State the blood parasite species.
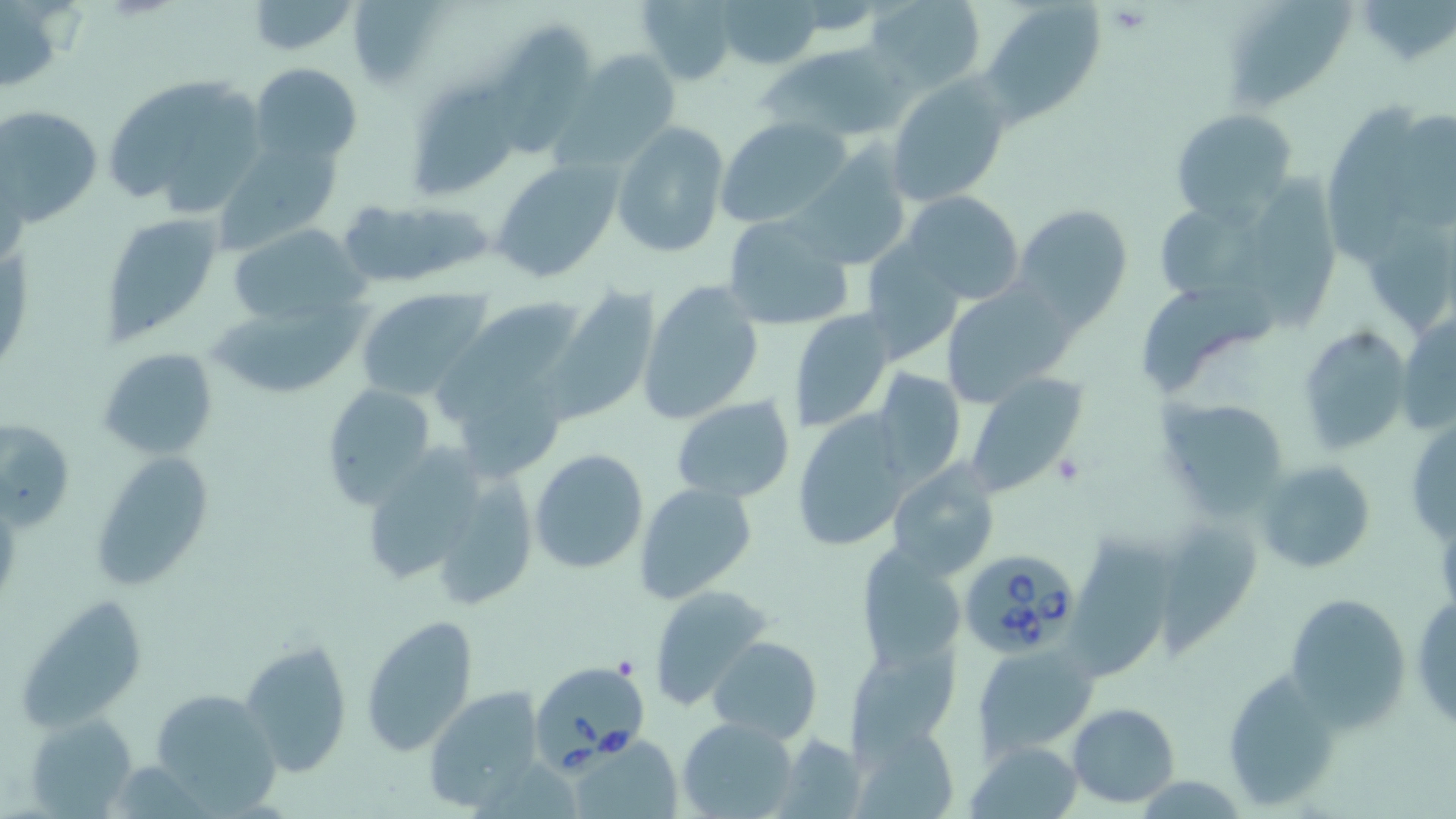
Babesia divergens.

Summary:
  - Coordinate format: approximate bounding boxes as (x1, y1, x2, y2) in pixels
  - Uninfected red blood cell locations: (348, 0, 449, 88), (635, 0, 742, 85), (716, 0, 825, 71), (865, 0, 988, 91), (1220, 0, 1358, 114), (244, 1, 360, 56), (1354, 1, 1455, 69), (981, 2, 1105, 124), (496, 24, 596, 159), (757, 40, 901, 141), (560, 51, 681, 167), (249, 63, 362, 166), (102, 72, 272, 215), (887, 76, 1011, 205), (411, 82, 519, 196), (1327, 103, 1429, 271), (0, 104, 103, 224), (1170, 109, 1297, 221), (1397, 112, 1456, 231), (717, 117, 853, 228), (612, 122, 730, 258), (214, 138, 344, 252), (794, 148, 911, 270), (490, 159, 623, 283), (1259, 172, 1344, 334), (902, 191, 1025, 306), (354, 199, 498, 289), (1159, 199, 1280, 304), (1014, 204, 1133, 328), (99, 212, 225, 344), (723, 214, 856, 331), (1361, 217, 1455, 338), (226, 223, 368, 327), (861, 243, 966, 365), (1140, 277, 1276, 394), (638, 280, 764, 425), (939, 280, 1078, 407), (548, 286, 662, 425), (356, 288, 491, 401), (205, 295, 366, 402), (458, 295, 589, 399), (788, 307, 896, 432), (1399, 313, 1456, 438), (1297, 327, 1411, 453), (98, 347, 219, 459), (442, 354, 573, 481), (869, 368, 966, 486), (963, 374, 1089, 495), (319, 382, 438, 509), (670, 394, 797, 503), (1162, 400, 1287, 515), (793, 410, 917, 553), (1, 417, 75, 531), (1405, 417, 1456, 548), (366, 442, 485, 582), (529, 448, 650, 575), (91, 452, 218, 592), (415, 459, 543, 610), (1254, 459, 1377, 575), (886, 462, 1001, 581), (634, 482, 758, 607), (1155, 514, 1263, 645), (1072, 527, 1174, 678), (857, 544, 967, 672), (648, 584, 772, 708), (1284, 591, 1413, 728), (1409, 592, 1456, 733), (19, 597, 150, 737), (358, 614, 480, 756), (707, 635, 822, 741), (240, 637, 353, 777), (848, 643, 959, 753), (973, 645, 1098, 755), (1219, 666, 1346, 810), (422, 686, 545, 810), (144, 689, 281, 813), (1066, 702, 1180, 806), (26, 713, 140, 815), (677, 716, 799, 818), (847, 722, 961, 819), (570, 733, 682, 818), (775, 734, 866, 818), (966, 740, 1085, 819), (471, 763, 580, 819)
  - Babesia divergens-infected red blood cell locations: (957, 547, 1081, 659), (532, 657, 650, 767)
  - Platelet locations: (1106, 3, 1151, 34), (1049, 452, 1087, 485)
  - Field of view: single
  - Preparation: thin blood film
  - Image size: 1456×819 pixels
  - Stain: May-Grünwald-Giemsa
  - Modality: optical microscopy
  - Magnification: 1000x